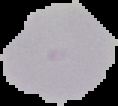

From a thin blood smear. Cell region segmented out of the field of view; the surrounding area is masked to black. Image is 118×106 pixels. Malaria status: uninfected.